State which parasite is depicted.
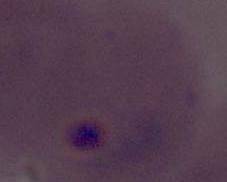
Plasmodium.

Summary:
  - Modality: photomicrograph
  - Magnification: 400x or 1000x